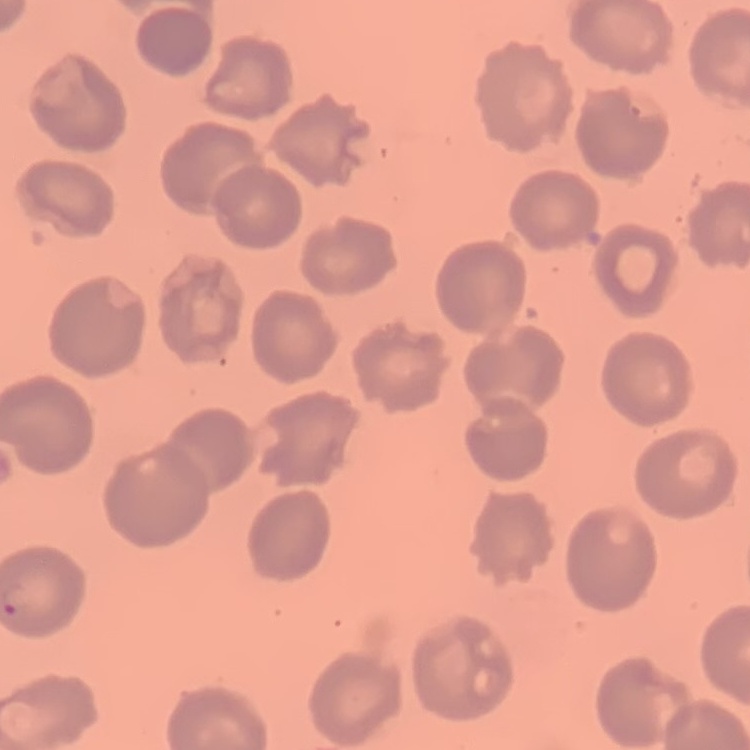
The red blood cells show no rouleaux formation. Thin peripheral smear. One tile cut from a larger photomicrograph. Stained with either Field's or Giemsa.